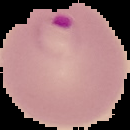

Summary:
  - Image type: segmented cell region on a black background
  - Preparation: thin blood smear
  - Image size: 130×130 pixels
  - Result: malaria parasites identified